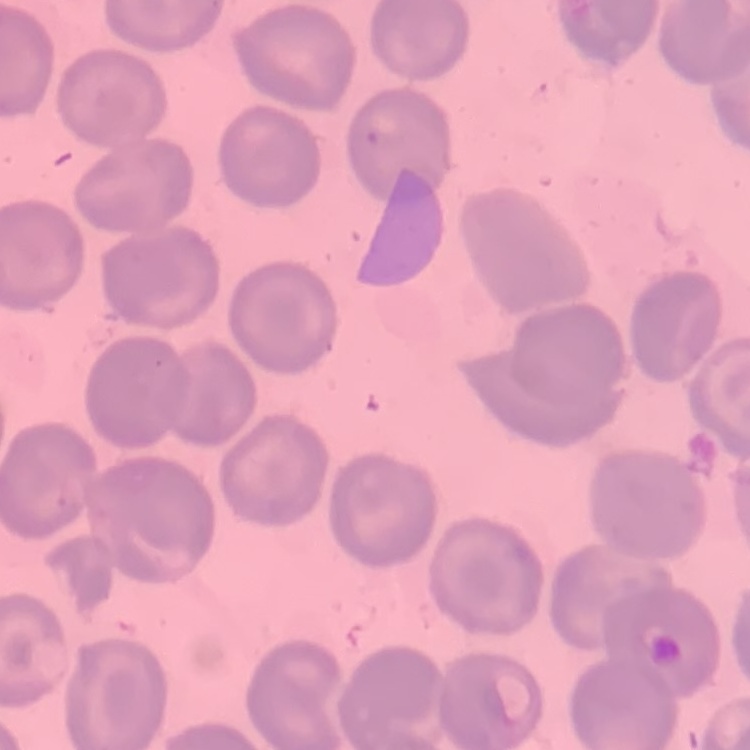 The red blood cells exhibit no rouleaux formation. Stained with either Field's or Giemsa. One tile cut from a larger photomicrograph. Thin peripheral smear.